Report the malaria status.
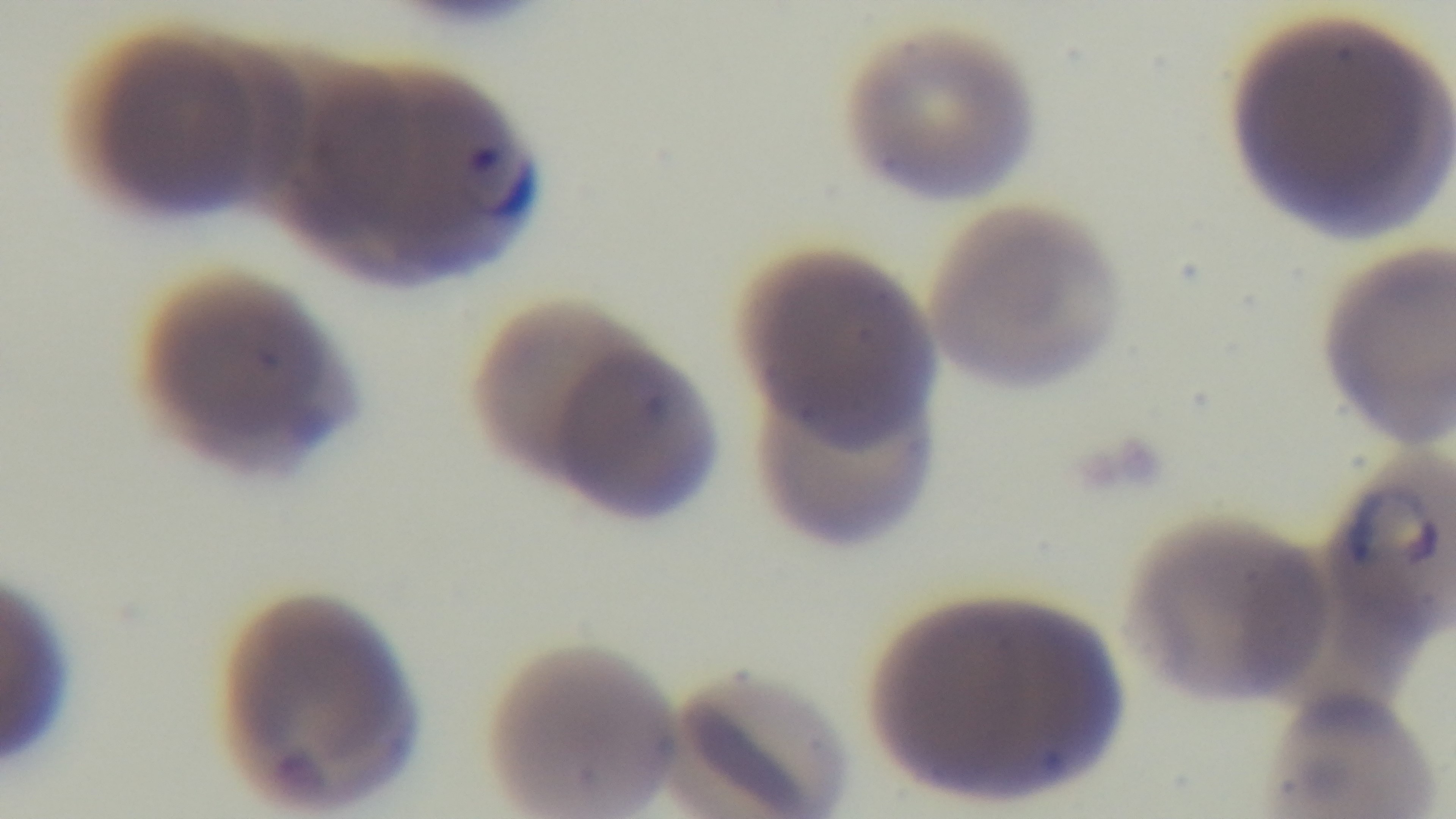
Infected.

{
  "field_of_view": "single",
  "stain": "Giemsa",
  "preparation": "thin blood film",
  "capture": "mounted 4K digital camera",
  "modality": "light microscopy",
  "objective": "100x oil immersion"
}